Assess this cell for malaria.
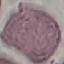
It is uninfected.

Photographed with a smartphone camera at the microscope eyepiece. Cell patch, automatically extracted from a larger field of view and resized to 64 × 64 pixels. Giemsa stain. Thin smear of blood.